Report the malaria status of this cell.
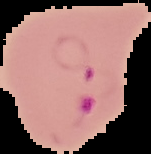
It is parasitized.

Cell region segmented out of the field of view; the surrounding area is masked to black. Image is 151×154 pixels. From a thin blood smear.